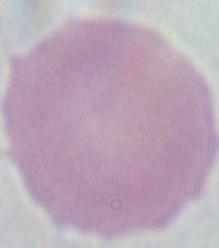

{
  "modality": "micrograph",
  "magnification": "1000x",
  "identification": "red blood cell"
}